Locate every Trypanosoma brucei.
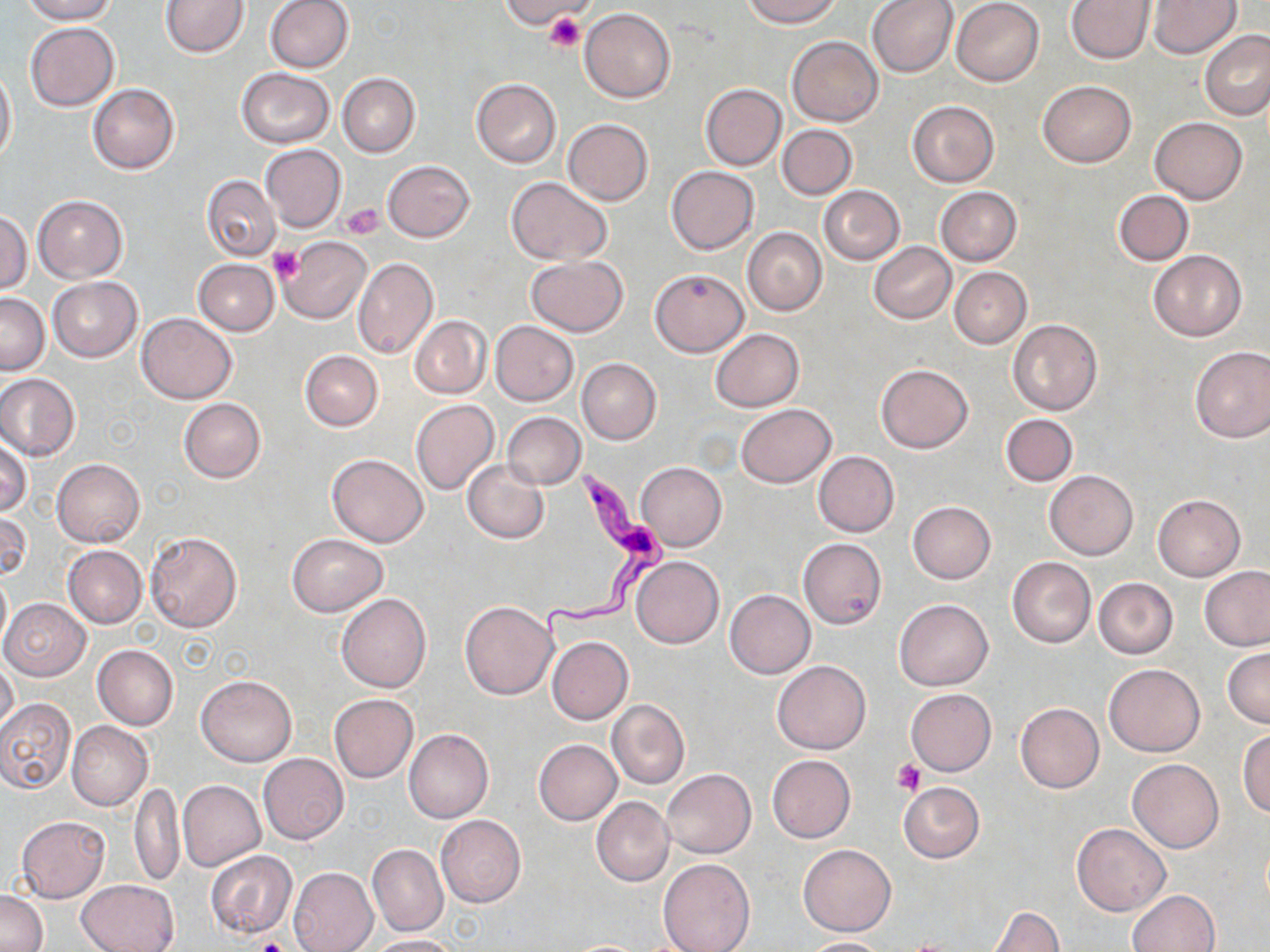
Approximate bounding boxes as (x1,y1)-(x2,y2) corner pairs in pixels.
Trypanosoma brucei: (539,468)-(672,641).

{
  "slide_level_diagnosis": "Trypanosoma brucei",
  "platelet_locations": "approximate bounding boxes as (x1,y1)-(x2,y2) corner pairs in pixels: (546,11)-(585,52), (344,202)-(383,239), (267,247)-(304,282), (893,760)-(925,796), (255,936)-(290,952)",
  "field_of_view": "one of a larger specimen",
  "image_size": "1270×952 pixels",
  "stain": "May-Grünwald-Giemsa",
  "preparation": "thin blood smear",
  "uninfected_red_blood_cell_locations": "approximate bounding boxes as (x1,y1)-(x2,y2) corner pairs in pixels: (21,0)-(117,24), (160,0)-(248,58), (264,0)-(354,73), (505,0)-(592,28), (866,0)-(959,77), (950,0)-(1044,86), (1065,0)-(1155,64), (1149,0)-(1241,58), (742,1)-(841,27), (579,8)-(677,103), (25,23)-(119,111), (1201,29)-(1270,121), (787,37)-(882,126), (0,65)-(17,164), (237,68)-(335,148), (337,73)-(420,157), (471,78)-(561,167), (1037,80)-(1137,167), (88,83)-(179,174), (701,84)-(786,169), (908,101)-(998,186), (1151,117)-(1248,203), (562,118)-(653,206), (777,124)-(857,199), (261,145)-(346,231), (383,160)-(474,242), (665,166)-(759,255), (201,175)-(281,260), (505,177)-(612,265), (819,185)-(904,265), (935,186)-(1022,267), (1115,189)-(1193,266), (34,195)-(127,282), (0,211)-(31,294), (742,228)-(827,317), (280,236)-(372,324), (869,242)-(956,323), (1148,249)-(1246,342), (525,255)-(629,337), (353,257)-(438,359), (194,260)-(279,336), (949,266)-(1031,347), (650,268)-(748,358), (48,278)-(142,361), (0,292)-(49,375), (136,313)-(237,404), (408,315)-(491,399), (1007,320)-(1102,416), (490,321)-(577,405), (711,328)-(803,412), (1189,345)-(1270,443), (299,349)-(384,431), (577,358)-(662,444), (876,364)-(973,453), (0,373)-(80,462), (178,398)-(266,483), (409,400)-(499,497), (736,404)-(836,486), (502,412)-(585,488), (1001,414)-(1077,487), (1,439)-(32,518), (814,452)-(899,536), (326,454)-(428,547), (52,458)-(145,547), (463,459)-(548,544), (635,463)-(727,549), (1044,469)-(1138,559), (1152,493)-(1246,580), (908,501)-(995,584), (0,511)-(30,582), (145,532)-(242,633), (286,533)-(388,616), (798,538)-(886,629), (62,545)-(146,628), (630,556)-(724,648), (1007,557)-(1096,647), (1199,565)-(1269,652), (0,569)-(11,653), (1093,577)-(1179,658), (724,590)-(815,678), (337,593)-(432,692), (1,598)-(90,680), (894,598)-(993,691), (459,600)-(557,699), (547,637)-(633,723), (92,644)-(178,730), (1223,646)-(1270,728), (1,657)-(18,737), (773,660)-(870,754), (1103,663)-(1205,756), (196,673)-(297,766), (905,689)-(994,775), (328,693)-(418,782), (0,697)-(76,794), (607,699)-(690,788), (1016,703)-(1104,792), (67,721)-(152,810), (1238,727)-(1270,817), (404,728)-(493,822), (534,739)-(622,825), (259,753)-(349,844), (767,755)-(855,842), (1128,759)-(1224,852), (662,769)-(756,858), (177,780)-(265,870), (130,781)-(185,888), (898,781)-(984,863), (591,798)-(673,886), (435,814)-(526,908), (15,817)-(110,902), (1071,822)-(1170,916), (798,844)-(896,935), (367,845)-(448,937), (205,850)-(297,938), (658,857)-(754,952), (289,866)-(378,952), (77,879)-(180,952), (1126,888)-(1220,951), (0,890)-(48,952), (986,906)-(1064,952), (370,935)-(461,952), (798,937)-(895,952), (559,939)-(658,951)",
  "modality": "optical microscopy",
  "magnification": "1000x"
}